Find each parasitized RBC.
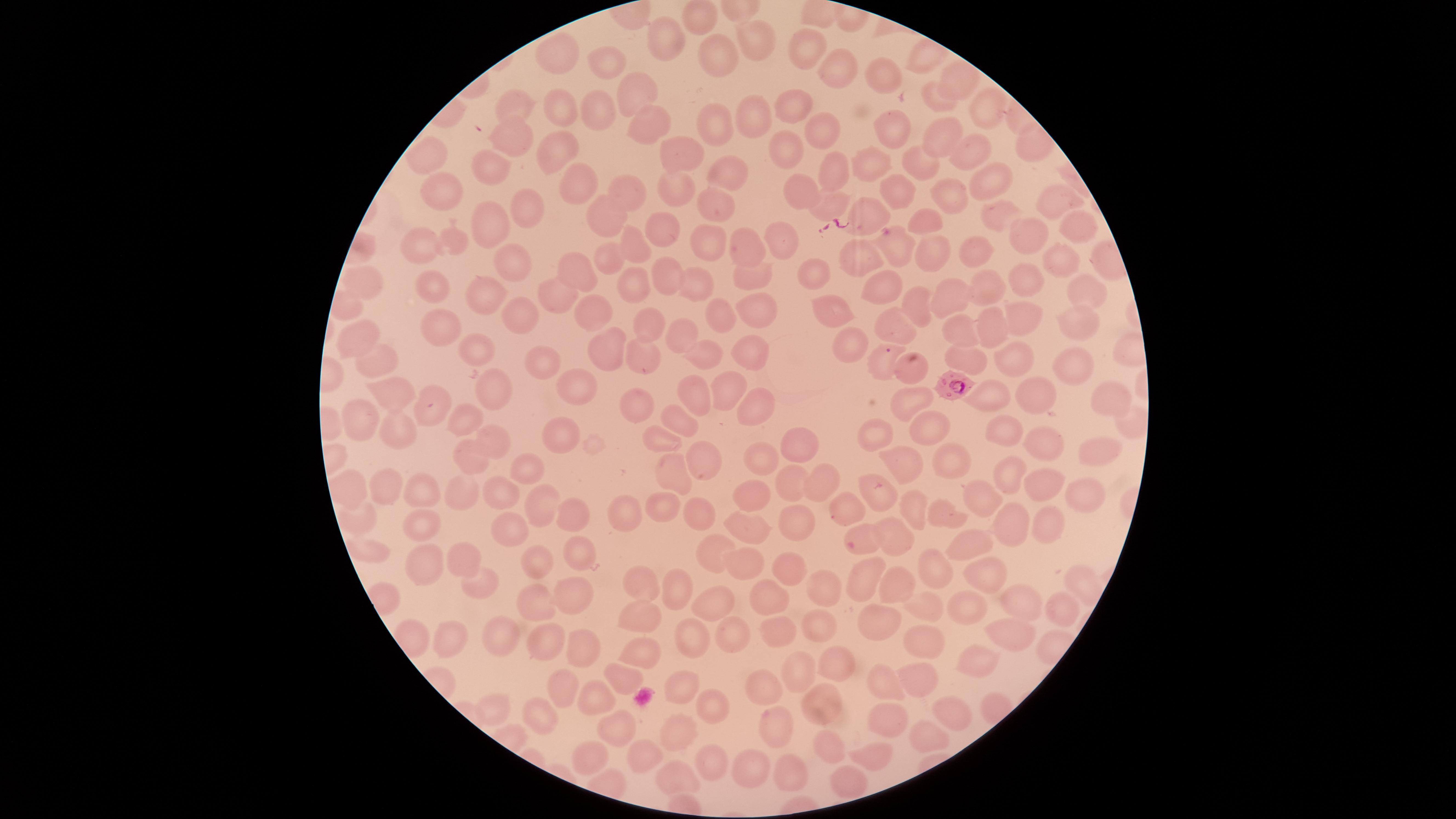

Approximate marker points as [x, y] in pixels.
Parasitized RBCs: [951, 384].

Approximate marker points as [x, y] in pixels. Uninfected RBCs: [704, 17], [669, 39], [761, 42], [812, 46], [559, 52], [722, 56], [607, 63], [834, 68], [887, 76], [957, 77], [634, 94], [939, 96], [514, 104], [791, 105], [601, 111], [558, 112], [988, 116], [754, 121], [649, 125], [718, 127], [892, 129], [825, 130], [938, 133], [510, 137], [682, 148], [791, 150], [968, 151], [554, 152], [428, 156], [871, 160], [926, 164], [489, 170], [834, 171], [731, 174], [989, 181], [575, 184], [674, 185], [799, 192], [895, 192], [948, 192], [446, 193], [628, 194], [1052, 202], [715, 204], [826, 205], [528, 207], [1003, 212], [925, 217], [869, 218], [610, 219], [492, 222], [1078, 229], [662, 232], [1029, 234], [714, 240], [456, 243], [424, 244], [779, 246], [640, 247], [746, 247], [897, 248], [932, 248], [979, 250], [511, 257], [611, 257], [858, 260], [1055, 262], [570, 271], [803, 273], [753, 275], [666, 278], [1025, 281], [699, 283], [430, 284], [636, 284], [365, 285], [875, 287], [986, 291], [486, 292], [1084, 292], [553, 294], [949, 295], [908, 301], [594, 307], [834, 308], [722, 311], [522, 312], [754, 312], [442, 318], [1029, 318], [650, 319], [1075, 320], [959, 325], [985, 325], [896, 327], [682, 331], [362, 334], [852, 341], [701, 346], [473, 349], [612, 349], [753, 351], [967, 356], [1015, 356], [643, 359], [544, 360], [878, 360], [376, 363], [912, 367], [1069, 370], [730, 385], [571, 386], [494, 388], [695, 388], [389, 395], [997, 396], [1045, 400], [433, 402], [643, 402], [910, 404], [1110, 405], [759, 412], [465, 419], [361, 423], [679, 423], [929, 428], [398, 429], [1001, 433], [878, 435], [559, 440], [660, 440], [493, 441], [797, 447], [1041, 451], [470, 455], [1092, 456], [703, 458], [759, 459], [947, 463], [903, 465], [527, 467], [1012, 474], [672, 476], [348, 483], [823, 483], [1046, 483], [794, 484], [502, 486], [386, 488], [881, 490], [421, 493], [1074, 493], [460, 494], [751, 494], [982, 496], [540, 498], [850, 501], [912, 504], [669, 506], [622, 510], [944, 514], [361, 515], [701, 515], [575, 518], [1045, 522], [512, 523], [794, 523], [1010, 524], [747, 526], [420, 527], [863, 533], [895, 535], [967, 545], [707, 549], [373, 552], [581, 554], [747, 555], [462, 557], [543, 561], [788, 568], [928, 568], [430, 570], [975, 575], [642, 578], [862, 582], [676, 584], [484, 585], [894, 587], [825, 588], [577, 591], [772, 594], [715, 599], [538, 600], [1010, 602], [924, 607], [977, 607], [1055, 612], [644, 615], [817, 625], [879, 628], [504, 630], [455, 631], [779, 631], [692, 632], [1011, 634], [731, 635], [924, 639], [539, 644], [585, 647], [643, 650], [834, 654], [976, 656], [627, 671], [795, 677], [915, 681], [881, 685], [563, 686], [681, 687], [764, 687], [822, 701], [605, 702], [497, 705], [713, 708], [952, 709], [546, 715], [885, 717], [622, 728], [782, 731], [680, 735], [925, 738], [828, 750], [591, 753], [646, 753], [877, 755], [709, 757], [749, 765], [680, 776], [784, 776], [846, 784]. The visible region is circular. Thin blood film. Image is 1456×819 pixels. Species: Plasmodium falciparum. Single field of view. Giemsa-stained preparation. Photographed with a smartphone camera through the microscope eyepiece.